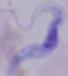

modality = micrograph
magnification = 1000x
identification = trypanosome